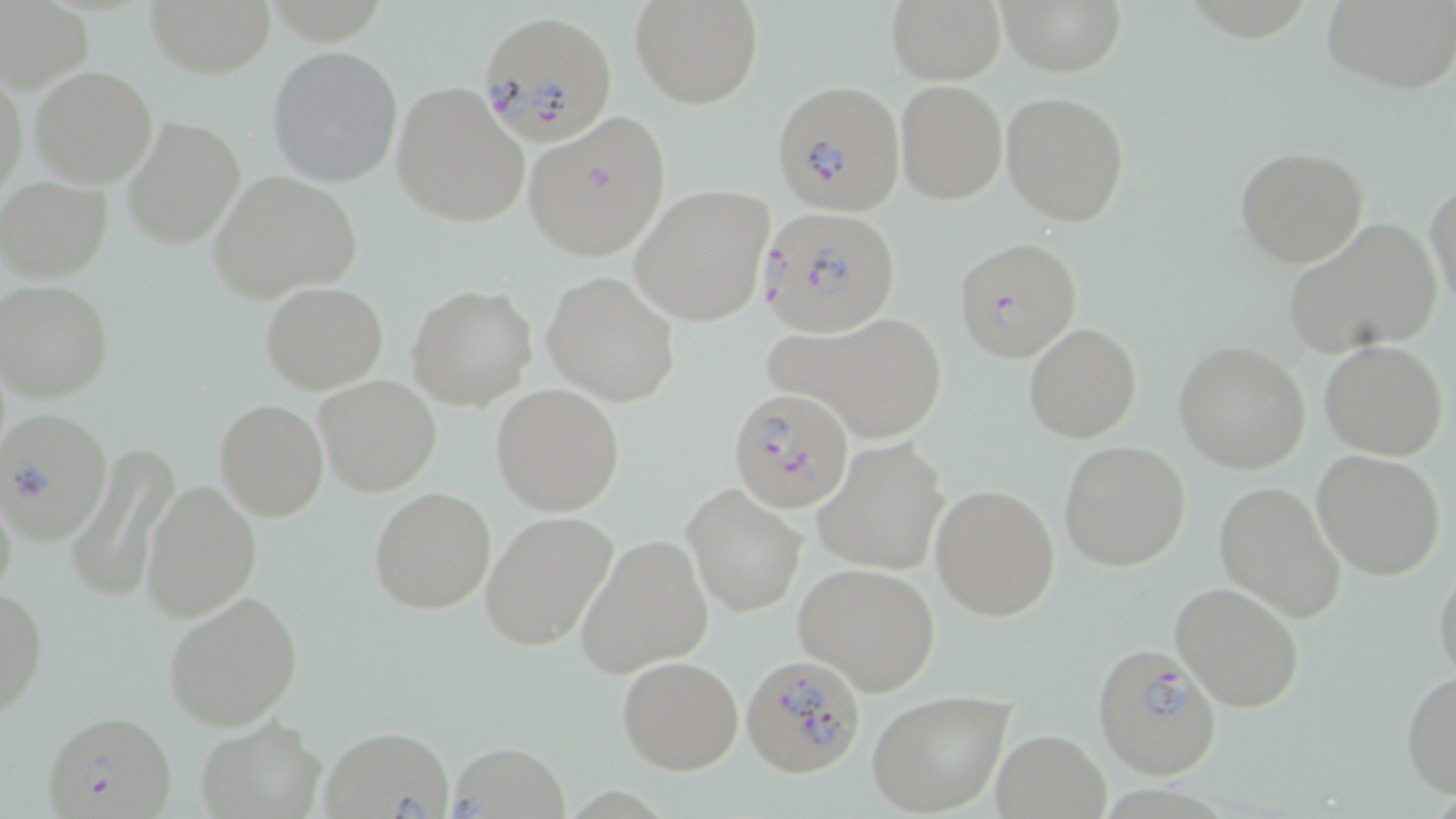
Summary:
  - Coordinate format: approximate bounding boxes as named x1/y1/x2/y2 corners in pixels
  - Plasmodium falciparum-infected red blood cell locations: (x1=477, y1=8, x2=616, y2=144), (x1=772, y1=78, x2=906, y2=215), (x1=759, y1=205, x2=901, y2=337), (x1=953, y1=236, x2=1081, y2=362), (x1=727, y1=387, x2=857, y2=515), (x1=1, y1=409, x2=113, y2=545), (x1=1091, y1=643, x2=1221, y2=780), (x1=741, y1=653, x2=867, y2=778), (x1=42, y1=710, x2=177, y2=819)
  - Uninfected red blood cell locations: (x1=143, y1=0, x2=275, y2=77), (x1=884, y1=0, x2=1006, y2=86), (x1=1323, y1=0, x2=1456, y2=91), (x1=0, y1=1, x2=93, y2=93), (x1=629, y1=1, x2=764, y2=110), (x1=1001, y1=1, x2=1125, y2=77), (x1=267, y1=44, x2=404, y2=189), (x1=30, y1=65, x2=159, y2=188), (x1=1, y1=66, x2=26, y2=203), (x1=896, y1=79, x2=1006, y2=203), (x1=390, y1=80, x2=532, y2=229), (x1=1000, y1=90, x2=1131, y2=228), (x1=521, y1=110, x2=672, y2=262), (x1=123, y1=114, x2=245, y2=250), (x1=1233, y1=144, x2=1367, y2=268), (x1=207, y1=171, x2=361, y2=301), (x1=0, y1=177, x2=112, y2=281), (x1=1426, y1=177, x2=1455, y2=315), (x1=631, y1=182, x2=776, y2=326), (x1=1284, y1=218, x2=1443, y2=358), (x1=541, y1=270, x2=681, y2=406), (x1=2, y1=279, x2=114, y2=402), (x1=260, y1=282, x2=387, y2=394), (x1=407, y1=284, x2=537, y2=411), (x1=768, y1=309, x2=952, y2=444), (x1=1023, y1=322, x2=1142, y2=442), (x1=1174, y1=340, x2=1312, y2=473), (x1=1320, y1=340, x2=1449, y2=459), (x1=314, y1=375, x2=441, y2=496), (x1=491, y1=385, x2=624, y2=515), (x1=214, y1=398, x2=329, y2=521), (x1=814, y1=435, x2=949, y2=577), (x1=1058, y1=439, x2=1191, y2=571), (x1=65, y1=441, x2=180, y2=606), (x1=1311, y1=450, x2=1446, y2=580), (x1=0, y1=474, x2=19, y2=613), (x1=141, y1=479, x2=262, y2=623), (x1=1213, y1=481, x2=1349, y2=625), (x1=929, y1=482, x2=1059, y2=621), (x1=683, y1=483, x2=808, y2=617), (x1=368, y1=487, x2=495, y2=614), (x1=480, y1=511, x2=619, y2=653), (x1=575, y1=534, x2=714, y2=677), (x1=1432, y1=560, x2=1456, y2=686), (x1=793, y1=561, x2=941, y2=695), (x1=1170, y1=582, x2=1305, y2=712), (x1=0, y1=585, x2=47, y2=717), (x1=162, y1=588, x2=304, y2=732), (x1=617, y1=655, x2=743, y2=774), (x1=1401, y1=669, x2=1456, y2=800), (x1=866, y1=691, x2=1015, y2=816), (x1=193, y1=715, x2=327, y2=819), (x1=320, y1=726, x2=457, y2=818), (x1=990, y1=730, x2=1110, y2=818), (x1=446, y1=742, x2=572, y2=817)
  - Slide-level diagnosis: Plasmodium falciparum
  - Modality: light microscopy
  - Stain: May-Grünwald-Giemsa
  - Magnification: 1000x
  - Image size: 1456×819 pixels
  - Preparation: thin blood smear
  - Field of view: single